Identify the preparation type.
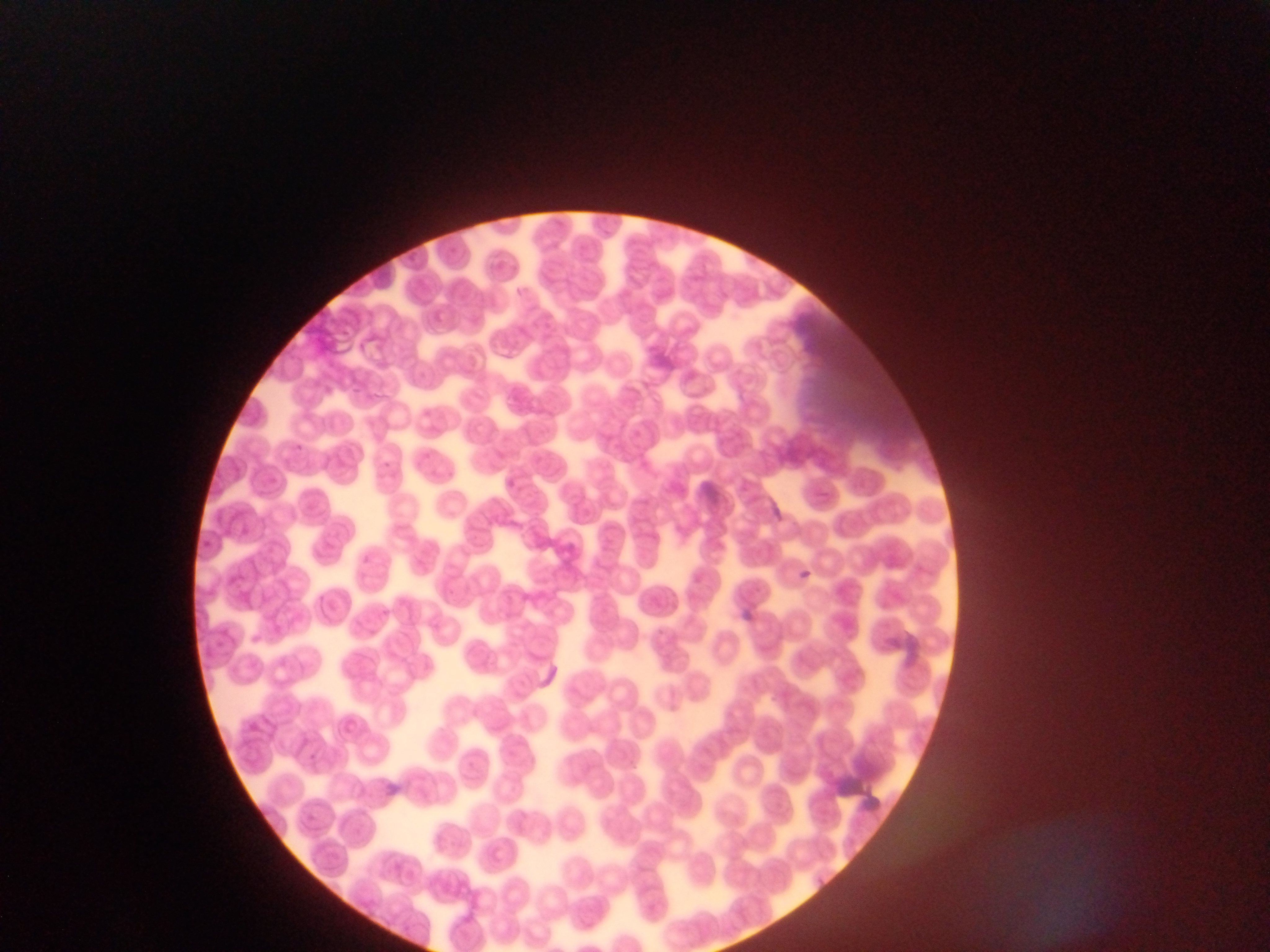

Thin blood film.

field of view = single
country = Ghana
malaria parasite locations = approximate bounding boxes as (left, top, right, bottom) in pixels: (296, 440, 312, 454), (793, 567, 815, 587)
image size = 1270×952 pixels
capture = mobile-phone photograph through a microscope